Assess for malaria.
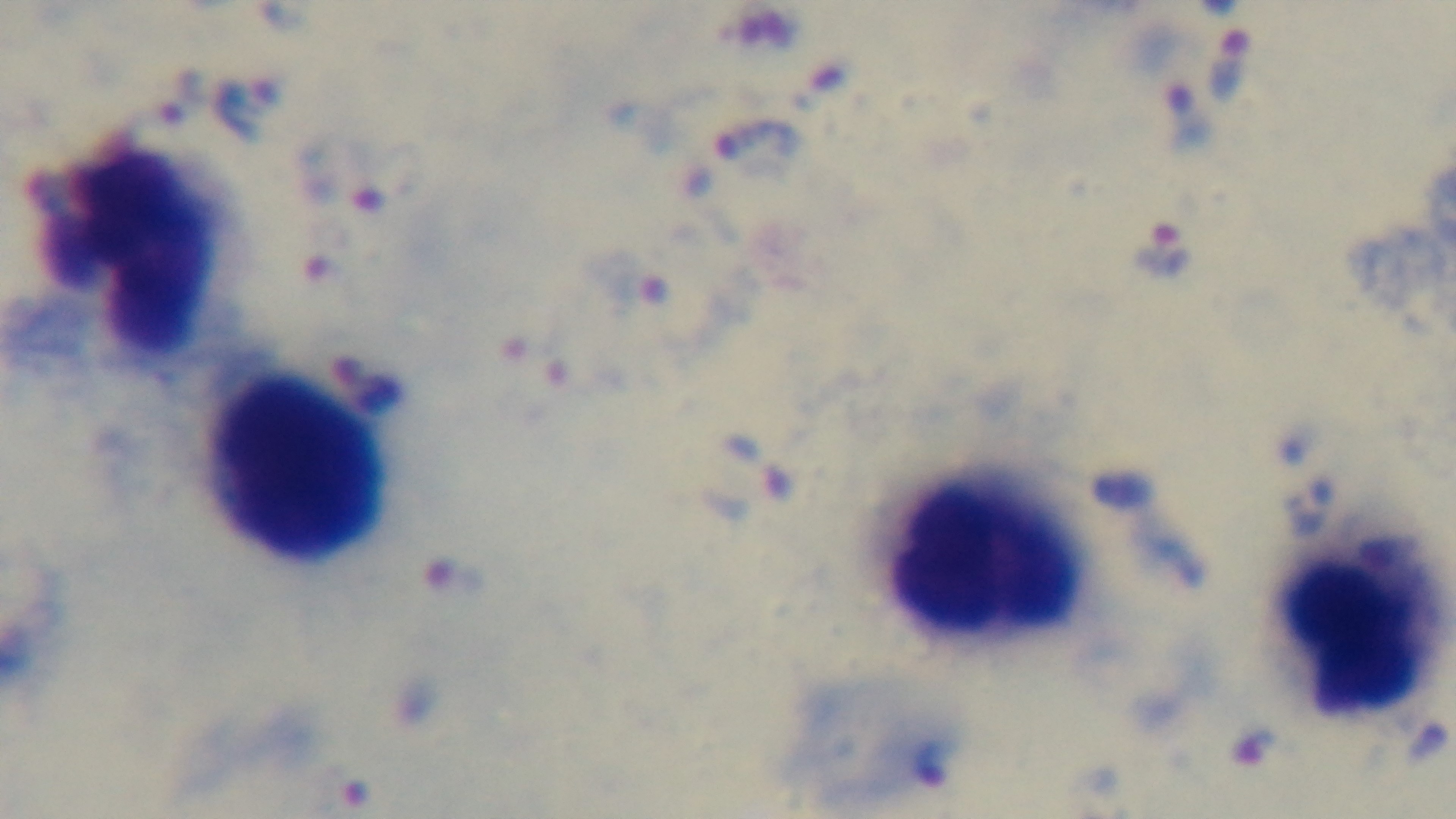

It is infected.

{
  "field_of_view": "one from the slide",
  "objective": "100x oil immersion",
  "stain": "Giemsa",
  "modality": "light microscopy",
  "capture": "mounted 4K digital camera",
  "preparation": "thick blood film"
}